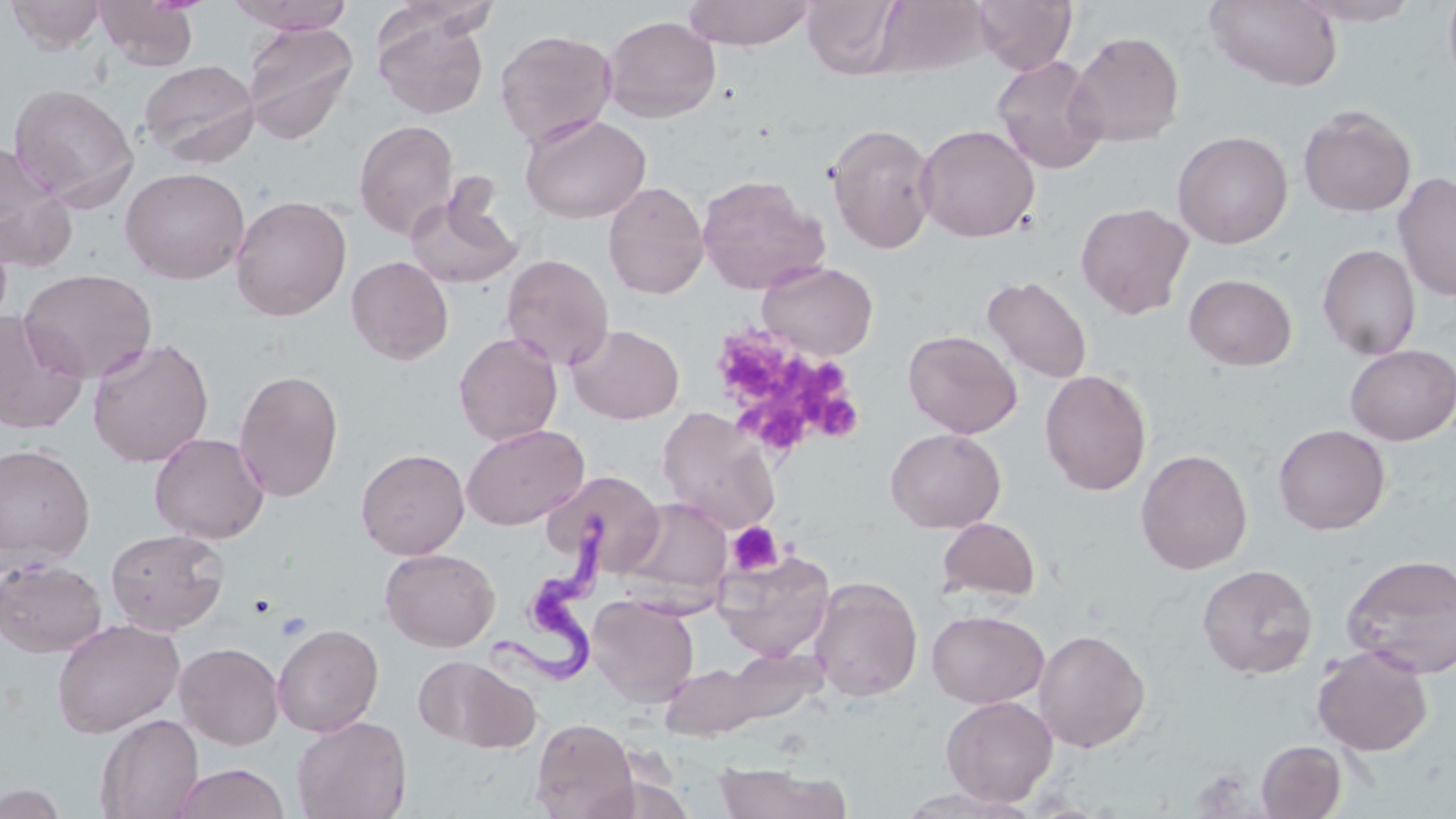 Approximate bounding boxes as (x1,y1)-(x2,y2) corner pairs in pixels. Platelet locations: (711,328)-(799,406), (794,364)-(847,408), (810,388)-(863,443), (751,407)-(802,451), (727,521)-(784,576). Uninfected red blood cell locations: (3,0)-(109,54), (226,0)-(357,32), (682,0)-(816,50), (804,0)-(905,79), (872,0)-(991,78), (973,0)-(1076,73), (1443,0)-(1456,94), (96,1)-(199,71), (1204,1)-(1343,90), (1293,1)-(1423,27), (373,10)-(490,120), (602,15)-(721,122), (242,20)-(359,145), (494,28)-(618,147), (1068,30)-(1185,147), (991,56)-(1108,174), (138,59)-(260,167), (8,84)-(139,209), (1298,105)-(1416,217), (519,112)-(651,224), (353,119)-(459,240), (826,123)-(939,254), (915,124)-(1040,243), (1173,130)-(1293,248), (0,141)-(75,270), (120,166)-(250,284), (1393,172)-(1456,303), (696,174)-(830,294), (603,181)-(709,299), (405,183)-(524,290), (229,194)-(351,321), (1075,202)-(1194,319), (1317,244)-(1421,360), (500,253)-(614,370), (346,255)-(453,364), (756,260)-(878,360), (19,268)-(157,383), (1184,273)-(1297,371), (982,275)-(1093,384), (1,312)-(88,434), (567,324)-(684,424), (902,330)-(1022,438), (453,331)-(563,445), (86,337)-(214,467), (1343,344)-(1456,445), (233,369)-(344,502), (1040,369)-(1152,495), (657,406)-(780,533), (461,423)-(589,530), (1273,423)-(1390,534), (885,427)-(1006,533), (149,432)-(269,544), (0,443)-(96,567), (356,448)-(469,559), (1136,449)-(1253,575), (546,469)-(657,573), (619,497)-(733,604), (936,517)-(1041,604), (105,528)-(229,635), (379,547)-(500,651), (712,549)-(836,661), (1341,553)-(1455,678), (0,557)-(107,657), (1197,563)-(1318,679), (808,576)-(923,702), (587,595)-(699,707), (926,608)-(1049,708), (51,618)-(184,738), (273,623)-(384,737), (1033,628)-(1150,752), (175,641)-(284,750), (1311,645)-(1433,756), (693,648)-(828,732), (415,654)-(540,753), (659,661)-(771,741), (940,695)-(1058,807), (95,713)-(204,819), (292,715)-(412,819), (531,717)-(638,819), (1256,740)-(1347,818), (712,762)-(850,819), (169,763)-(292,819), (586,771)-(698,819), (0,783)-(69,819), (895,787)-(1040,819). Trypanosoma brucei locations: (484,513)-(610,694). Slide-level diagnosis: Trypanosoma brucei. Light microscopy. One field of a larger specimen. Captured at 1000x magnification. Thin blood film. Image is 1456×819 pixels. May-Grünwald-Giemsa stain.